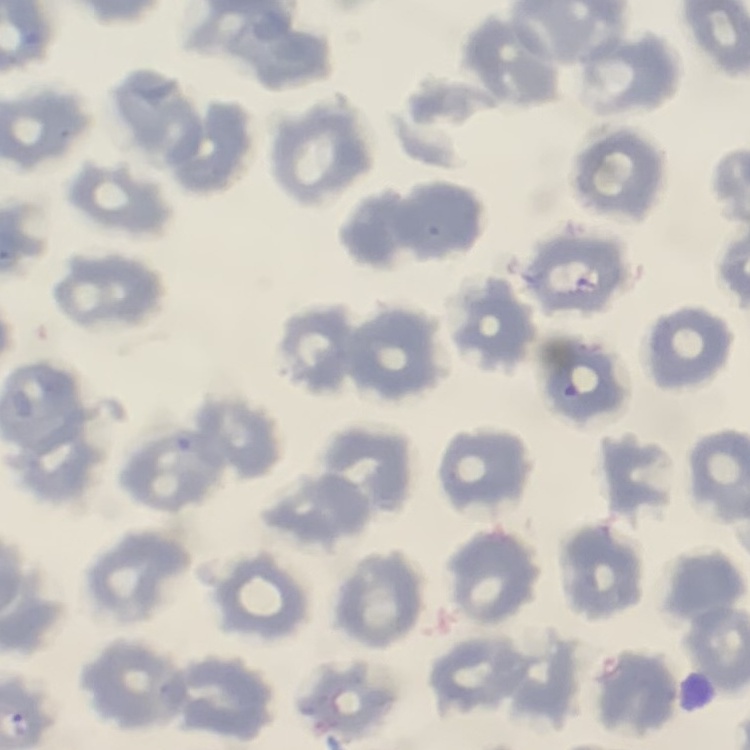
Summary:
  - Erythrocyte morphology: no rouleaux formation
  - Preparation: thin peripheral smear
  - Image type: one tile cut from a larger photomicrograph
  - Stain: Field's or Giemsa